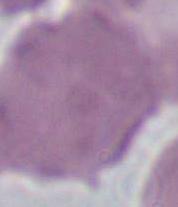 Photomicrograph. An erythrocyte is seen. Captured at 1000x magnification.